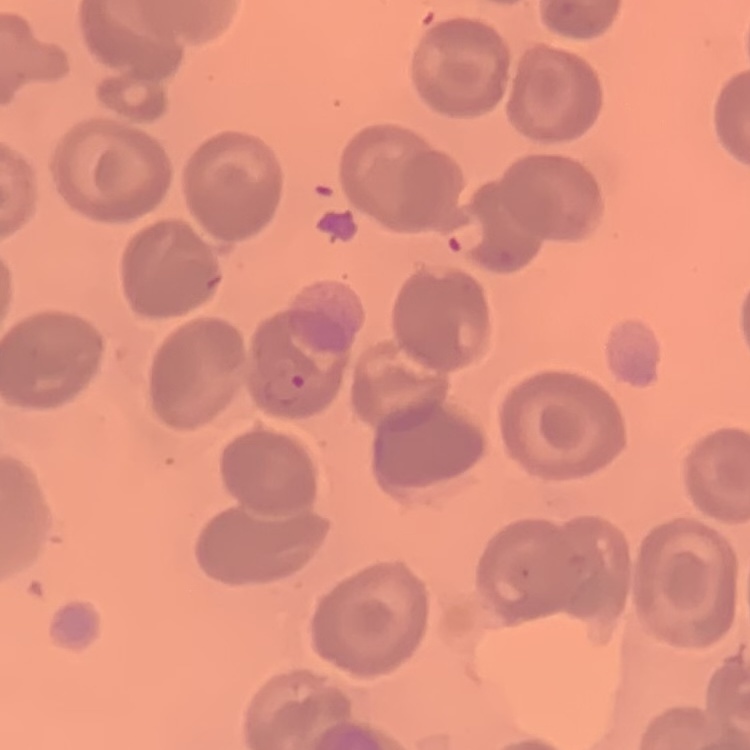
erythrocyte_morphology: no rouleaux formation
image_type: one tile cut from a larger photomicrograph
stain: Field's or Giemsa
preparation: thin peripheral smear